Describe the morphology of the red blood cells.
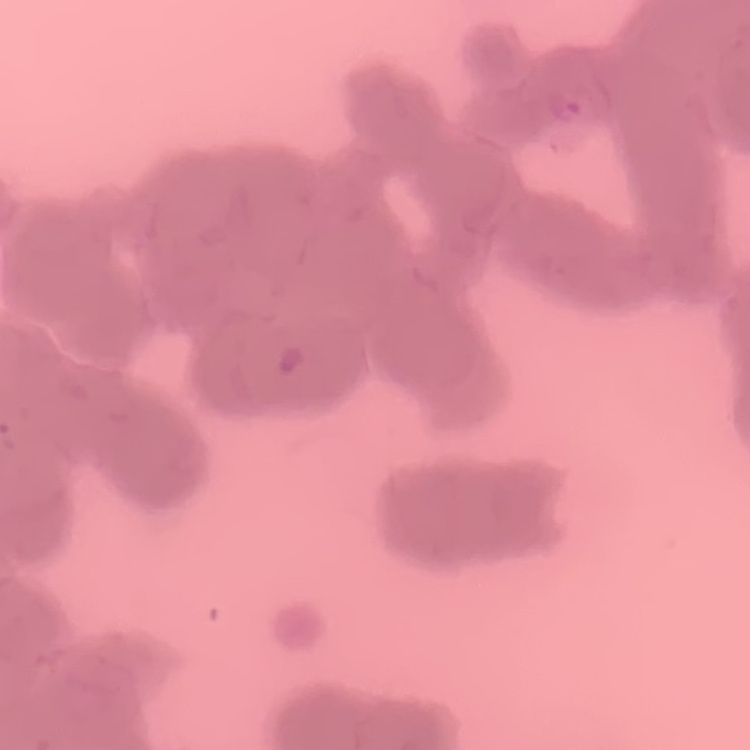
They show rouleaux formation.

image type = square crop of a larger photomicrograph
stain = Field's or Giemsa
preparation = thin blood smear